Assess the morphology of the red blood cells.
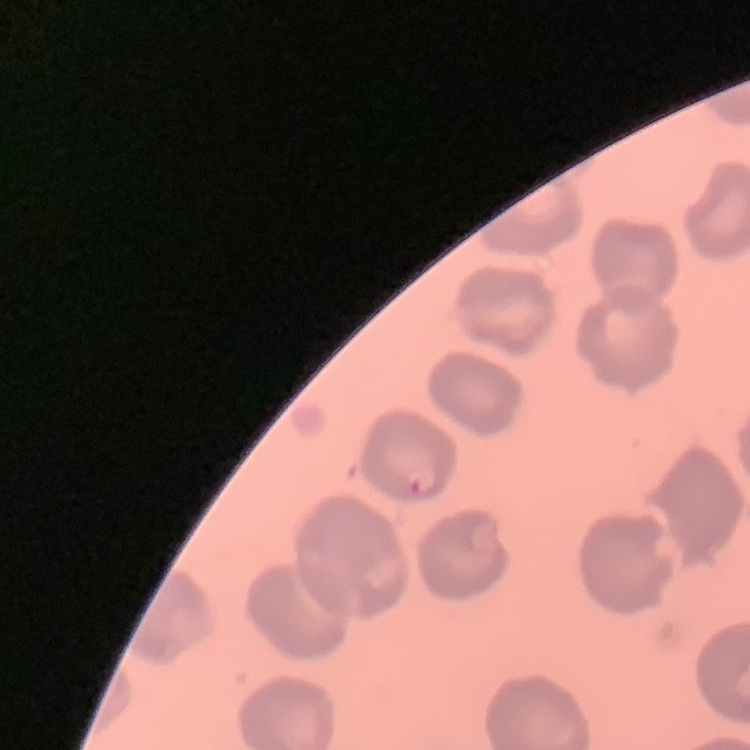

They show no rouleaux formation.

Summary:
  - Preparation: thin blood film
  - Image type: one tile cut from a larger photomicrograph
  - Stain: Field's or Giemsa